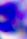

identification = white blood cell
modality = micrograph
magnification = 400x